Assess this cell for malaria.
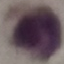
It is uninfected.

Summary:
  - Stain: Giemsa
  - Preparation: thin blood film
  - Image type: cell patch, automatically extracted from a larger field of view and resized to 64 × 64 pixels
  - Capture: smartphone camera at the microscope eyepiece